Assess this cell for malaria.
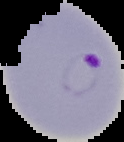

Parasitized.

Cell region segmented out of the field of view; the surrounding area is masked to black. From a thin blood film. Image is 124×142 pixels.